Describe the morphology of the red blood cells.
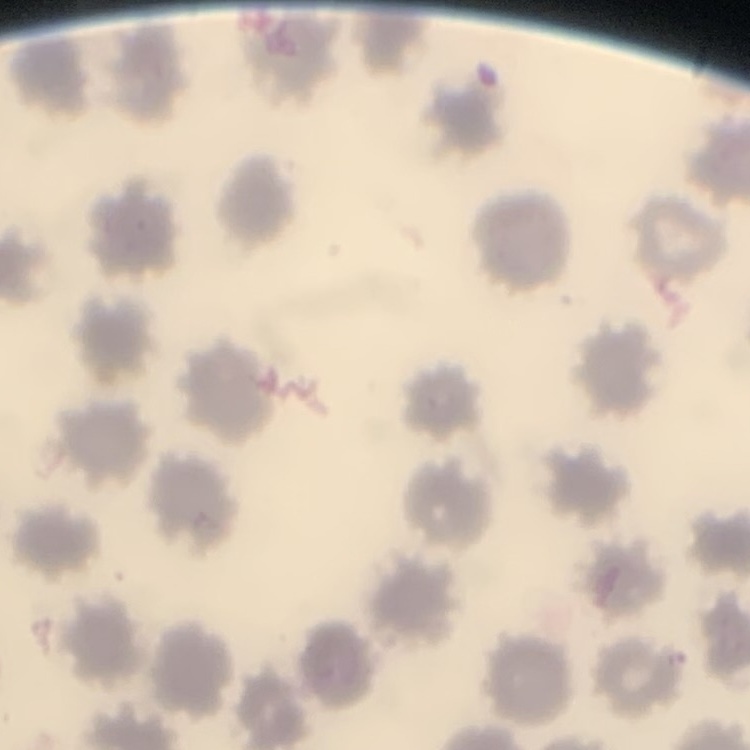

No rouleaux formation.

stain = Field's or Giemsa
image type = square crop of a larger photomicrograph
preparation = thin blood smear